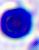
identification = white blood cell
magnification = 400x
modality = photomicrograph